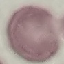
malaria status = uninfected
capture = smartphone through the microscope eyepiece
stain = Giemsa
preparation = thin blood smear
image type = automatically extracted cell patch, resized to 64 × 64 pixels